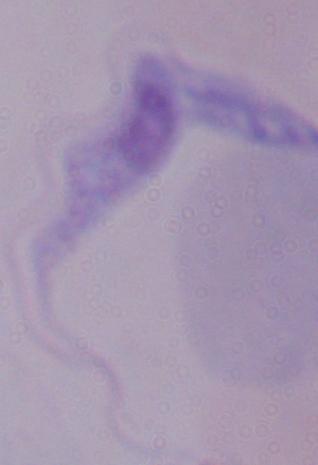

modality = micrograph
magnification = 1000x
identification = trypanosome